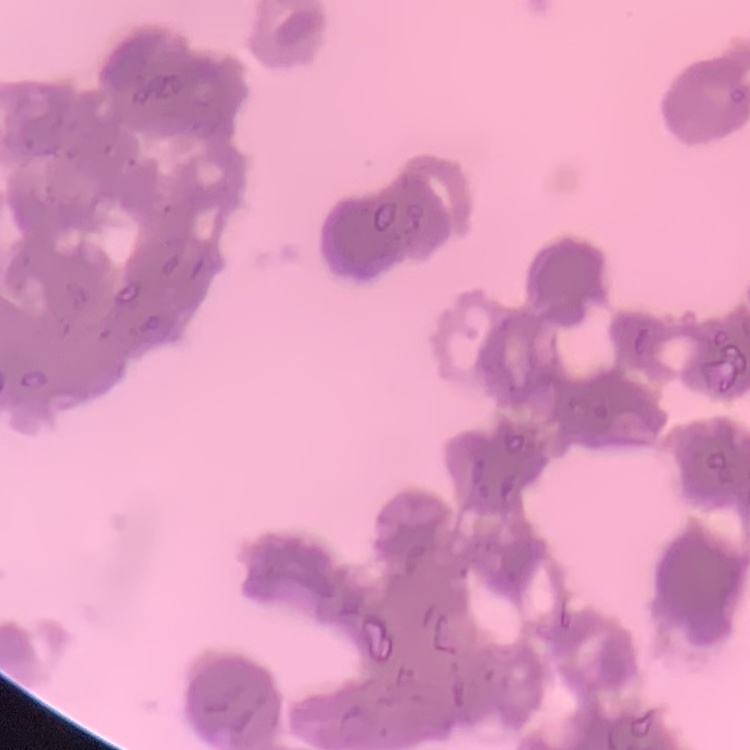

Summary:
  - Erythrocyte morphology: rouleaux formation
  - Preparation: thin blood film
  - Image type: square crop of a larger photomicrograph
  - Stain: Field's or Giemsa